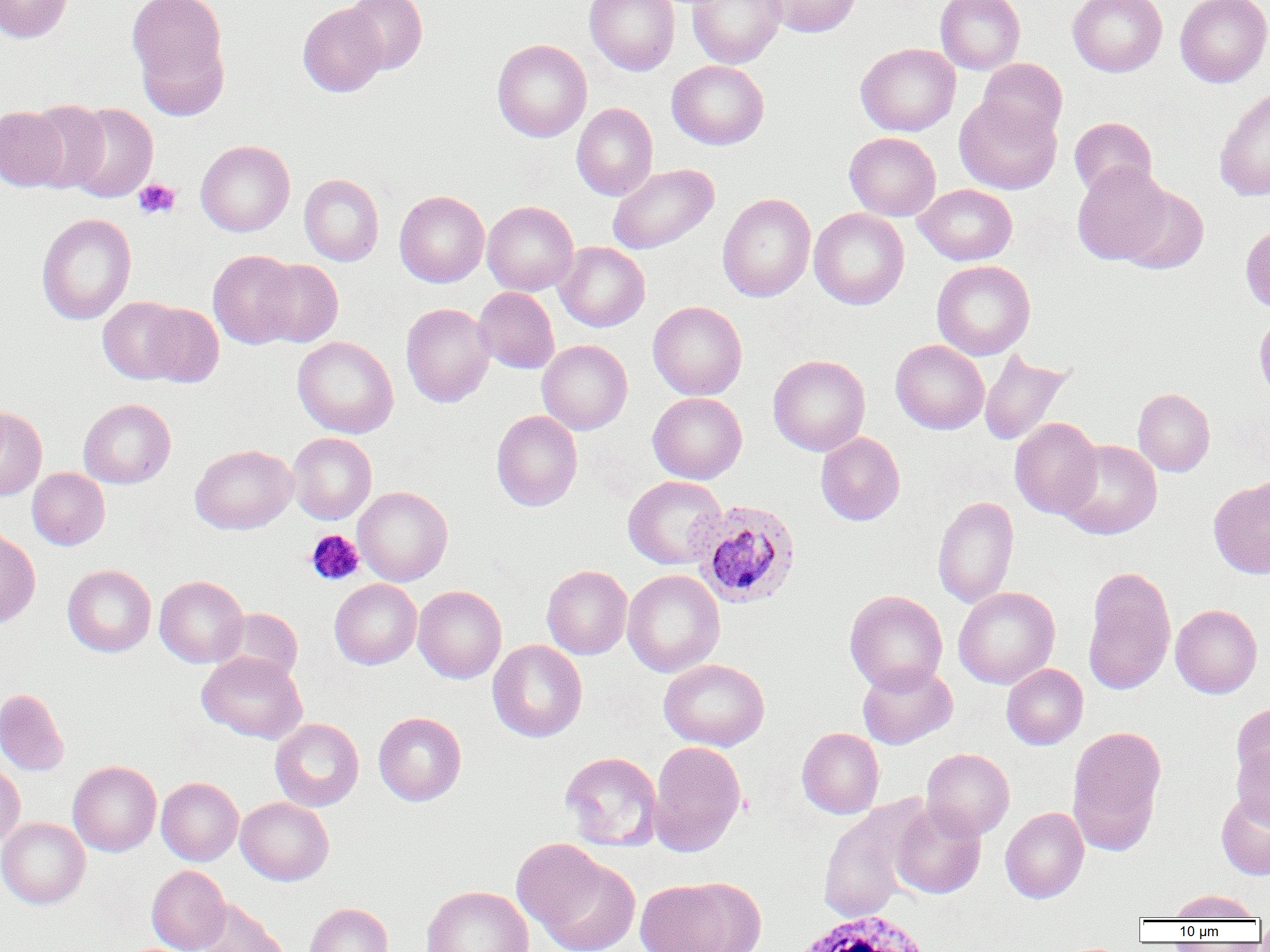
Summary:
  - Coordinate format: approximate bounding boxes as named x1/y1/x2/y2 corners in pixels
  - Platelet locations: (x1=133, y1=179, x2=181, y2=219), (x1=305, y1=529, x2=364, y2=585)
  - Plasmodium ovale-infected red blood cell locations: (x1=690, y1=498, x2=801, y2=609)
  - Uninfected red blood cell locations: (x1=0, y1=0, x2=73, y2=43), (x1=127, y1=0, x2=230, y2=108), (x1=342, y1=0, x2=427, y2=75), (x1=585, y1=0, x2=680, y2=75), (x1=687, y1=0, x2=785, y2=68), (x1=763, y1=0, x2=861, y2=37), (x1=935, y1=0, x2=1025, y2=74), (x1=1067, y1=0, x2=1167, y2=77), (x1=1175, y1=0, x2=1270, y2=88), (x1=298, y1=3, x2=387, y2=96), (x1=492, y1=38, x2=592, y2=142), (x1=855, y1=43, x2=961, y2=136), (x1=977, y1=58, x2=1067, y2=143), (x1=667, y1=60, x2=769, y2=150), (x1=1214, y1=85, x2=1270, y2=202), (x1=954, y1=96, x2=1061, y2=195), (x1=25, y1=99, x2=110, y2=192), (x1=571, y1=102, x2=658, y2=201), (x1=65, y1=103, x2=158, y2=203), (x1=0, y1=105, x2=68, y2=191), (x1=1069, y1=117, x2=1157, y2=198), (x1=844, y1=132, x2=941, y2=221), (x1=195, y1=140, x2=295, y2=236), (x1=1071, y1=163, x2=1172, y2=265), (x1=607, y1=164, x2=719, y2=254), (x1=299, y1=173, x2=384, y2=266), (x1=913, y1=184, x2=1018, y2=266), (x1=1117, y1=185, x2=1208, y2=275), (x1=394, y1=190, x2=489, y2=287), (x1=717, y1=193, x2=815, y2=301), (x1=482, y1=200, x2=578, y2=295), (x1=809, y1=208, x2=909, y2=310), (x1=36, y1=213, x2=136, y2=325), (x1=1240, y1=222, x2=1270, y2=314), (x1=555, y1=241, x2=650, y2=331), (x1=208, y1=249, x2=302, y2=349), (x1=255, y1=259, x2=343, y2=347), (x1=932, y1=260, x2=1035, y2=360), (x1=473, y1=287, x2=559, y2=374), (x1=98, y1=295, x2=188, y2=384), (x1=647, y1=300, x2=748, y2=400), (x1=140, y1=303, x2=224, y2=387), (x1=400, y1=303, x2=495, y2=408), (x1=292, y1=336, x2=398, y2=438), (x1=537, y1=340, x2=632, y2=435), (x1=890, y1=340, x2=989, y2=435), (x1=978, y1=349, x2=1073, y2=446), (x1=768, y1=354, x2=870, y2=456), (x1=1132, y1=388, x2=1215, y2=477), (x1=648, y1=392, x2=747, y2=484), (x1=78, y1=398, x2=176, y2=488), (x1=0, y1=406, x2=47, y2=500), (x1=492, y1=410, x2=582, y2=511), (x1=1009, y1=417, x2=1103, y2=519), (x1=288, y1=432, x2=377, y2=524), (x1=815, y1=432, x2=905, y2=526), (x1=1057, y1=439, x2=1162, y2=539), (x1=190, y1=443, x2=297, y2=534), (x1=27, y1=468, x2=110, y2=550), (x1=1250, y1=471, x2=1270, y2=546), (x1=623, y1=475, x2=726, y2=569), (x1=1209, y1=479, x2=1270, y2=580), (x1=353, y1=486, x2=453, y2=587), (x1=932, y1=495, x2=1019, y2=609), (x1=0, y1=528, x2=40, y2=628), (x1=62, y1=564, x2=156, y2=657), (x1=542, y1=565, x2=632, y2=659), (x1=1082, y1=567, x2=1176, y2=694), (x1=622, y1=569, x2=725, y2=677), (x1=154, y1=575, x2=248, y2=667), (x1=330, y1=579, x2=422, y2=669), (x1=413, y1=586, x2=507, y2=684), (x1=953, y1=586, x2=1060, y2=689), (x1=844, y1=589, x2=948, y2=694), (x1=1170, y1=604, x2=1262, y2=698), (x1=213, y1=607, x2=303, y2=686), (x1=487, y1=640, x2=588, y2=742), (x1=197, y1=652, x2=307, y2=744), (x1=659, y1=658, x2=769, y2=751), (x1=856, y1=662, x2=958, y2=749), (x1=1001, y1=663, x2=1088, y2=750), (x1=0, y1=688, x2=69, y2=776), (x1=1231, y1=703, x2=1270, y2=788), (x1=373, y1=711, x2=467, y2=806), (x1=270, y1=718, x2=364, y2=811), (x1=1067, y1=725, x2=1167, y2=854), (x1=797, y1=727, x2=884, y2=818), (x1=647, y1=740, x2=747, y2=856), (x1=1233, y1=744, x2=1270, y2=830), (x1=921, y1=748, x2=1015, y2=839), (x1=560, y1=751, x2=663, y2=851), (x1=68, y1=760, x2=161, y2=856), (x1=0, y1=761, x2=25, y2=848), (x1=156, y1=776, x2=243, y2=865), (x1=1216, y1=792, x2=1270, y2=880), (x1=236, y1=797, x2=333, y2=885), (x1=889, y1=800, x2=987, y2=899), (x1=817, y1=804, x2=921, y2=923), (x1=1000, y1=807, x2=1089, y2=903), (x1=0, y1=817, x2=90, y2=908), (x1=519, y1=844, x2=640, y2=951), (x1=147, y1=865, x2=230, y2=952), (x1=635, y1=878, x2=758, y2=952), (x1=421, y1=885, x2=534, y2=952), (x1=1169, y1=889, x2=1259, y2=921), (x1=194, y1=899, x2=289, y2=951), (x1=304, y1=902, x2=393, y2=952), (x1=1056, y1=943, x2=1128, y2=952)
  - White blood cell locations: (x1=783, y1=913, x2=942, y2=951)
  - Slide-level diagnosis: Plasmodium ovale
  - Image size: 1270×952 pixels
  - Preparation: thin blood smear
  - Modality: light microscopy
  - Field of view: single
  - Magnification: 1000x